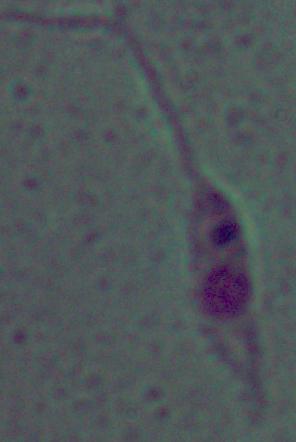

A Leishmania parasite is shown. Photomicrograph. 1000x magnification.